Identify the blood parasite species.
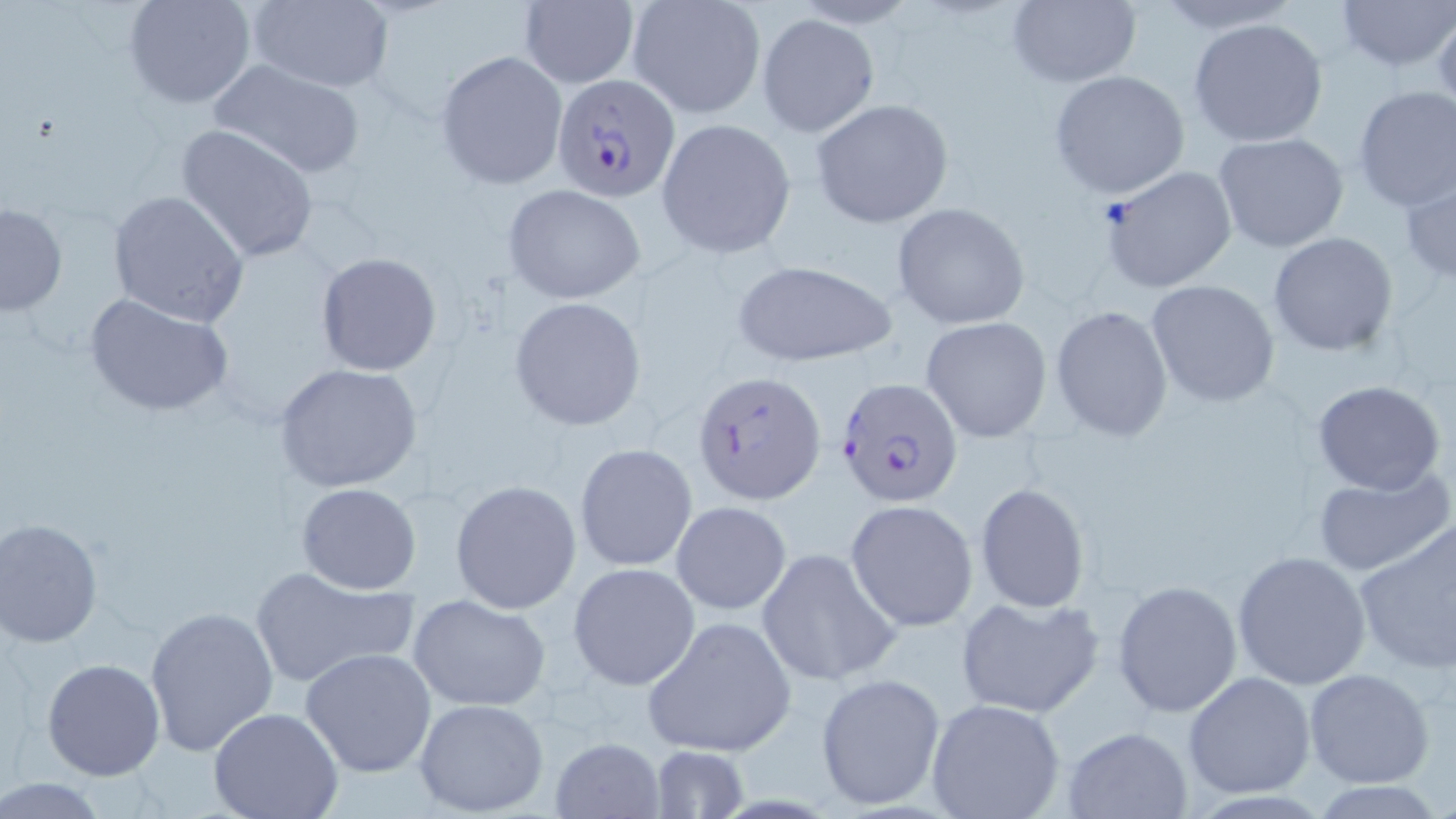
Plasmodium falciparum.

Summary:
  - Coordinate format: approximate bounding boxes as named x1/y1/x2/y2 corners in pixels
  - Plasmodium falciparum-infected red blood cell locations: (x1=552, y1=72, x2=679, y2=203), (x1=691, y1=371, x2=826, y2=504), (x1=833, y1=376, x2=962, y2=507)
  - Uninfected red blood cell locations: (x1=124, y1=0, x2=257, y2=108), (x1=517, y1=0, x2=638, y2=89), (x1=1335, y1=0, x2=1455, y2=71), (x1=245, y1=1, x2=393, y2=92), (x1=1006, y1=1, x2=1142, y2=88), (x1=625, y1=2, x2=765, y2=118), (x1=757, y1=13, x2=879, y2=137), (x1=1188, y1=17, x2=1328, y2=147), (x1=435, y1=49, x2=568, y2=189), (x1=207, y1=57, x2=368, y2=179), (x1=1049, y1=70, x2=1189, y2=199), (x1=1352, y1=88, x2=1456, y2=211), (x1=809, y1=98, x2=954, y2=229), (x1=656, y1=117, x2=796, y2=259), (x1=176, y1=124, x2=320, y2=262), (x1=1212, y1=131, x2=1350, y2=253), (x1=1099, y1=164, x2=1236, y2=292), (x1=1401, y1=171, x2=1456, y2=286), (x1=502, y1=183, x2=645, y2=306), (x1=107, y1=189, x2=252, y2=327), (x1=1, y1=202, x2=68, y2=316), (x1=891, y1=202, x2=1030, y2=329), (x1=1269, y1=231, x2=1399, y2=356), (x1=316, y1=251, x2=441, y2=376), (x1=726, y1=260, x2=897, y2=367), (x1=1144, y1=278, x2=1279, y2=409), (x1=85, y1=294, x2=231, y2=417), (x1=510, y1=296, x2=647, y2=432), (x1=1049, y1=305, x2=1174, y2=440), (x1=921, y1=315, x2=1053, y2=443), (x1=275, y1=363, x2=422, y2=492), (x1=1312, y1=381, x2=1446, y2=495), (x1=574, y1=443, x2=697, y2=572), (x1=1311, y1=467, x2=1455, y2=578), (x1=450, y1=480, x2=582, y2=612), (x1=296, y1=482, x2=422, y2=595), (x1=975, y1=483, x2=1093, y2=613), (x1=846, y1=499, x2=979, y2=632), (x1=671, y1=500, x2=793, y2=615), (x1=2, y1=519, x2=105, y2=648), (x1=1352, y1=519, x2=1456, y2=673), (x1=756, y1=546, x2=900, y2=685), (x1=1232, y1=550, x2=1371, y2=690), (x1=568, y1=562, x2=700, y2=689), (x1=248, y1=564, x2=418, y2=689), (x1=1112, y1=578, x2=1242, y2=716), (x1=408, y1=594, x2=552, y2=711), (x1=955, y1=594, x2=1104, y2=719), (x1=146, y1=604, x2=280, y2=756), (x1=642, y1=615, x2=796, y2=758), (x1=300, y1=647, x2=439, y2=777), (x1=41, y1=658, x2=165, y2=780), (x1=1305, y1=668, x2=1435, y2=787), (x1=1182, y1=671, x2=1316, y2=797), (x1=814, y1=673, x2=944, y2=810), (x1=411, y1=697, x2=551, y2=816), (x1=925, y1=697, x2=1066, y2=819), (x1=209, y1=708, x2=345, y2=819), (x1=1059, y1=727, x2=1195, y2=818), (x1=552, y1=736, x2=665, y2=818), (x1=646, y1=745, x2=751, y2=818), (x1=0, y1=778, x2=110, y2=815)
  - Field of view: one of a larger specimen
  - Modality: light microscopy
  - Preparation: thin blood smear
  - Stain: May-Grünwald-Giemsa
  - Magnification: 1000x
  - Image size: 1456×819 pixels